Report the malaria status of this cell.
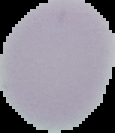

It is uninfected.

preparation: thin blood film
image_size: 115×133 pixels
image_type: segmented cell region with the area outside set to black